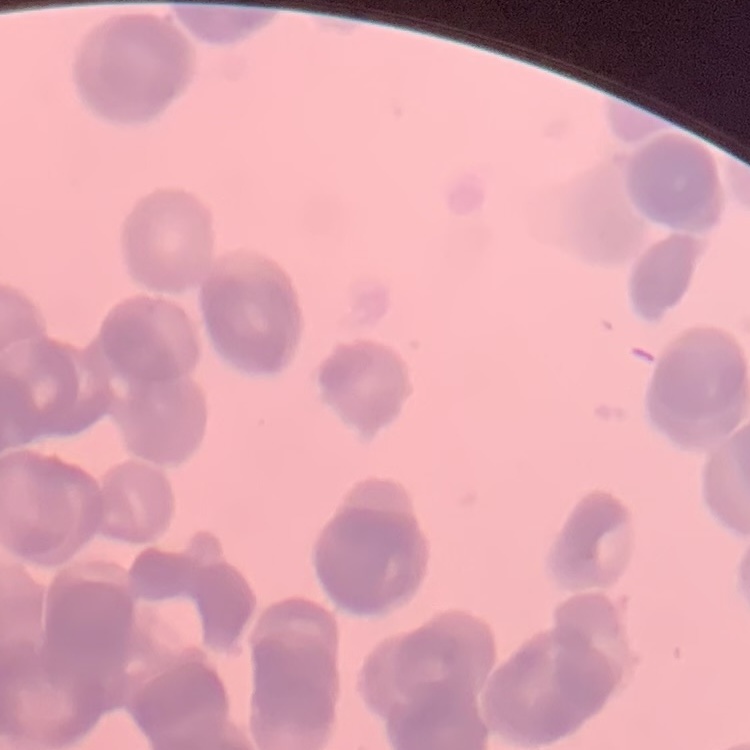

The erythrocytes exhibit rouleaux formation. Field's or Giemsa stain. Thin blood smear. Square crop of a larger photomicrograph.